State which cell type is depicted.
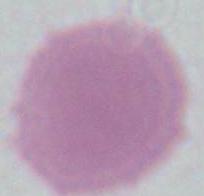
This is an erythrocyte.

Micrograph. 1000x magnification.